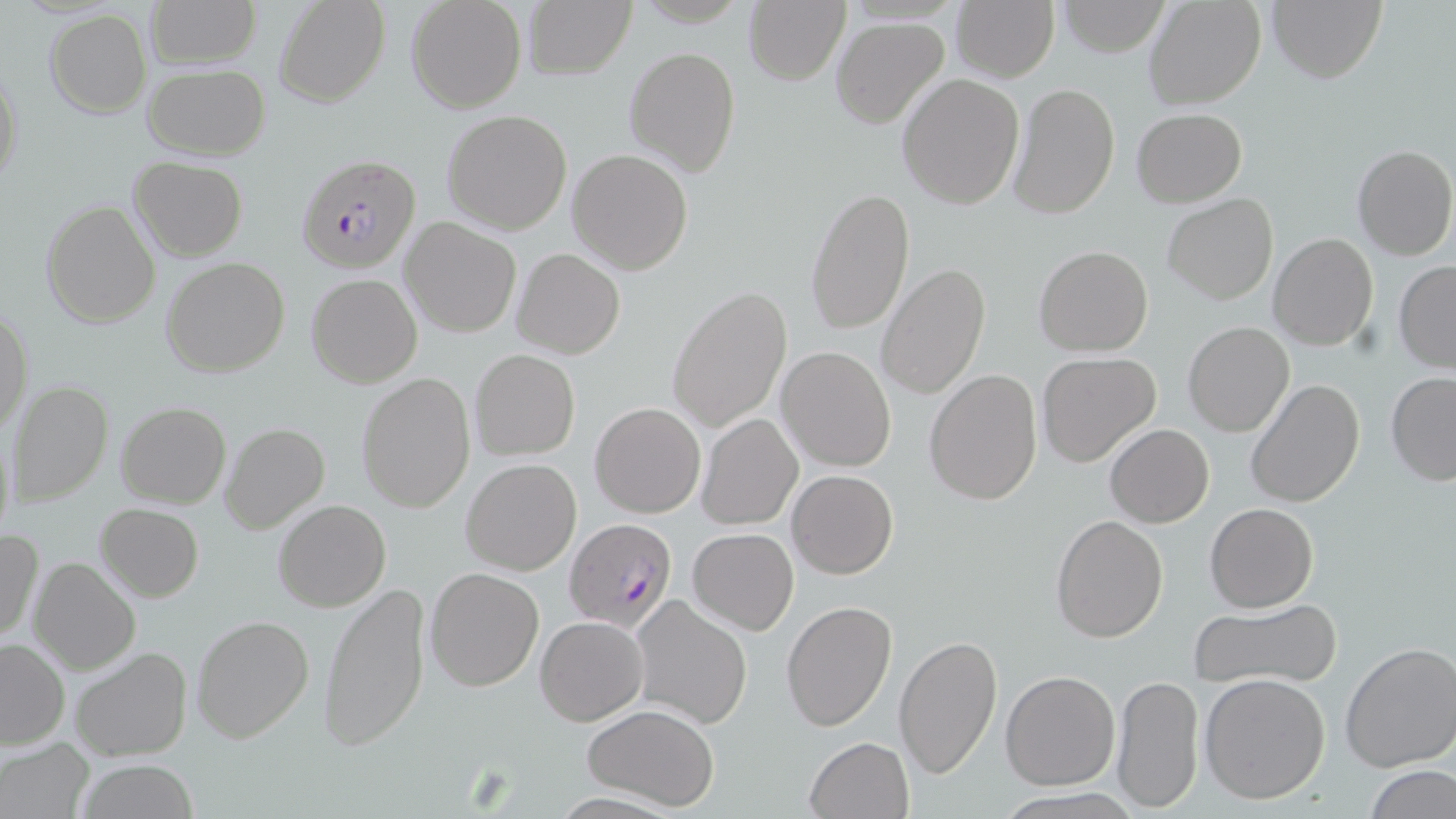

slide-level diagnosis = Plasmodium falciparum
field of view = one of a larger specimen
image size = 1456×819 pixels
modality = optical microscopy
uninfected red blood cell locations = approximate bounding boxes as [x1, y1, x2, y2] in pixels: [146, 0, 261, 69], [275, 0, 391, 106], [406, 0, 526, 113], [522, 0, 636, 80], [743, 0, 850, 86], [950, 0, 1059, 83], [1050, 0, 1175, 56], [1144, 0, 1267, 110], [1267, 0, 1387, 84], [45, 9, 151, 117], [831, 17, 949, 129], [625, 46, 740, 177], [0, 62, 23, 193], [142, 63, 269, 159], [896, 73, 1023, 211], [1008, 80, 1120, 220], [1131, 106, 1247, 205], [440, 109, 572, 234], [1352, 143, 1455, 261], [567, 148, 694, 276], [128, 156, 248, 261], [806, 187, 915, 336], [1163, 193, 1279, 305], [41, 199, 161, 329], [400, 218, 520, 337], [1268, 232, 1378, 351], [1033, 245, 1154, 356], [512, 248, 625, 359], [161, 257, 291, 376], [1394, 259, 1456, 374], [877, 263, 989, 399], [306, 274, 422, 389], [666, 284, 793, 434], [0, 306, 33, 436], [1183, 320, 1294, 436], [777, 346, 896, 471], [469, 349, 580, 460], [1035, 351, 1161, 467], [924, 367, 1043, 507], [355, 371, 476, 514], [1385, 372, 1456, 486], [1245, 377, 1365, 507], [7, 381, 114, 506], [116, 400, 231, 509], [591, 402, 706, 517], [698, 412, 803, 529], [1, 418, 15, 553], [219, 422, 331, 536], [1104, 424, 1214, 527], [459, 458, 582, 575], [787, 469, 898, 580], [273, 499, 391, 612], [1205, 502, 1318, 613], [96, 503, 204, 601], [1049, 514, 1168, 643], [687, 528, 798, 636], [0, 529, 44, 643], [27, 557, 140, 675], [424, 566, 545, 692], [319, 579, 433, 753], [630, 593, 753, 731], [1188, 597, 1343, 690], [781, 599, 897, 732], [190, 614, 313, 744], [535, 615, 648, 726], [892, 633, 1003, 781], [0, 637, 70, 749], [1337, 641, 1456, 772], [70, 646, 193, 762], [1000, 671, 1120, 790], [1199, 673, 1331, 804], [1112, 675, 1204, 810], [581, 703, 720, 812], [804, 736, 913, 819], [0, 737, 95, 819], [75, 759, 201, 818], [1361, 765, 1454, 819], [995, 789, 1138, 819]
preparation = thin blood film
Plasmodium falciparum-infected red blood cell locations = approximate bounding boxes as [x1, y1, x2, y2] in pixels: [296, 153, 421, 274], [564, 520, 678, 634]
magnification = 1000x
stain = May-Grünwald-Giemsa